Point out each leukocyte.
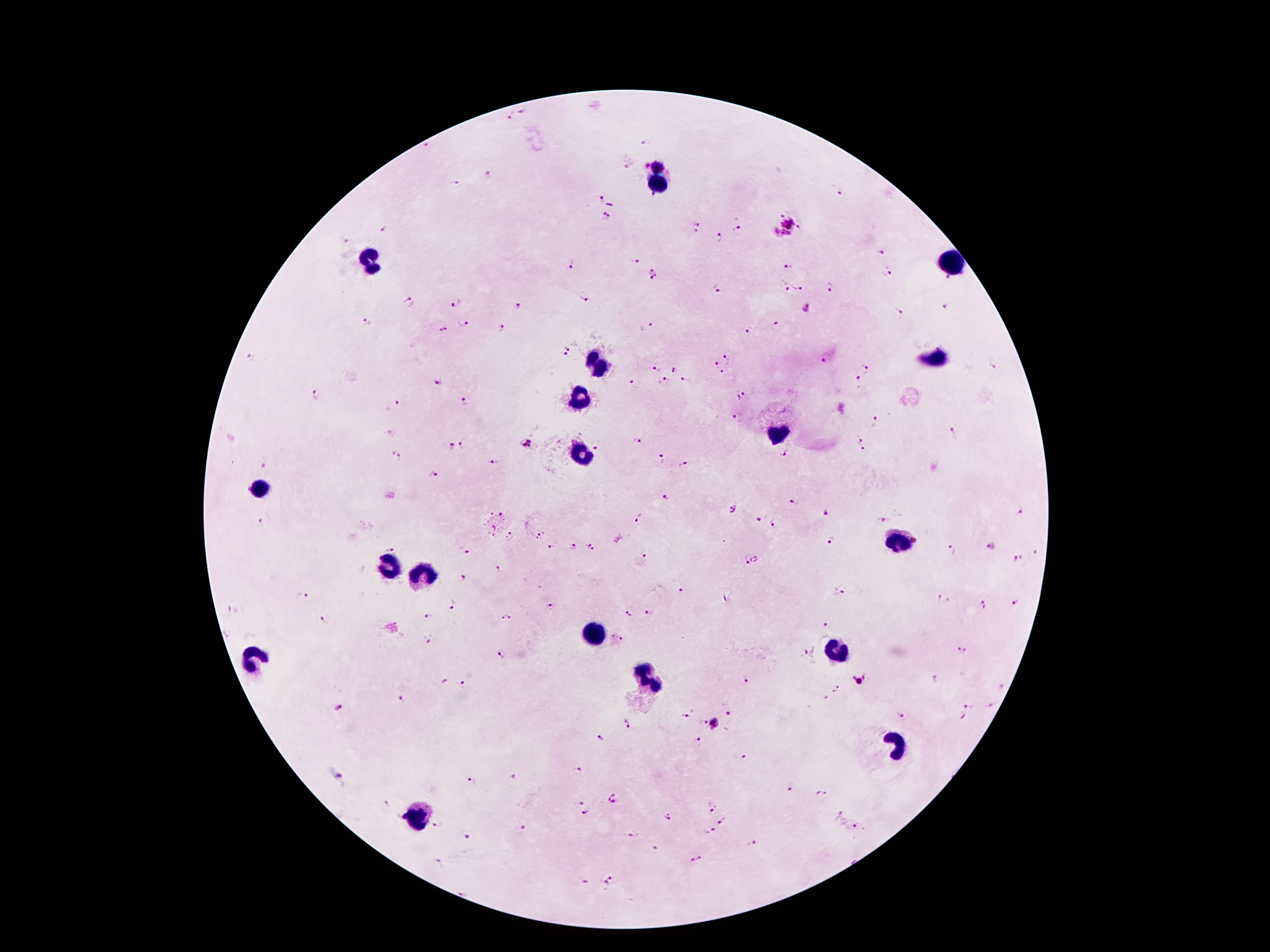

Approximate centers as (x, y) in pixels.
Leukocytes: (658, 184), (369, 260), (950, 263), (936, 360), (598, 363), (577, 398), (778, 434), (581, 454), (260, 487), (898, 539), (388, 565), (420, 574), (593, 635), (835, 651), (253, 656), (644, 677), (896, 745), (420, 817).

Summary:
  - Malaria parasite locations: (523, 111), (509, 117), (643, 141), (427, 145), (658, 168), (487, 177), (455, 181), (600, 201), (604, 216), (781, 216), (788, 225), (799, 227), (697, 228), (737, 228), (384, 230), (721, 237), (344, 241), (881, 252), (635, 261), (571, 266), (789, 268), (887, 273), (656, 275), (947, 280), (784, 285), (797, 288), (830, 288), (717, 289), (584, 299), (409, 303), (457, 304), (517, 306), (944, 306), (807, 309), (899, 314), (464, 323), (778, 323), (366, 324), (647, 326), (442, 329), (502, 331), (749, 332), (569, 346), (563, 356), (727, 356), (253, 358), (824, 358), (715, 364), (992, 367), (655, 369), (866, 369), (673, 370), (720, 372), (436, 379), (683, 380), (855, 380), (664, 381), (633, 383), (316, 396), (741, 396), (465, 403), (395, 406), (736, 418), (875, 422), (955, 434), (859, 440), (636, 441), (526, 443), (462, 444), (596, 446), (451, 447), (393, 451), (863, 451), (784, 454), (399, 457), (658, 460), (492, 462), (683, 465), (264, 466), (432, 473), (668, 497), (791, 502), (737, 510), (829, 513), (1021, 513), (264, 519), (638, 519), (757, 519), (880, 519), (771, 523), (540, 535), (511, 539), (832, 540), (573, 546), (992, 546), (551, 547), (589, 547), (389, 548), (463, 551), (951, 551), (644, 556), (755, 559), (1017, 559), (745, 560), (499, 571), (461, 578), (842, 591), (680, 592), (305, 596), (944, 599), (1014, 601), (454, 605), (983, 605), (549, 608), (232, 612), (629, 613), (649, 613), (428, 615), (506, 618), (326, 622), (825, 623), (620, 638), (428, 639), (961, 647), (500, 654), (807, 654), (859, 679), (933, 680), (746, 681), (466, 684), (1003, 686), (837, 689), (401, 698), (969, 704), (993, 705), (339, 709), (686, 715), (902, 715), (729, 716), (962, 718), (624, 723), (713, 723), (600, 738), (697, 742), (743, 756), (577, 771), (337, 776), (513, 778), (473, 782), (790, 786), (819, 793), (615, 801), (387, 802), (579, 802), (708, 808), (839, 814), (584, 815), (668, 819), (723, 822), (437, 826), (522, 828), (856, 828), (709, 830), (466, 836), (632, 836), (753, 844), (654, 848), (698, 858), (436, 860), (611, 879), (584, 882), (463, 892)
  - Patient malaria status: positive for Plasmodium falciparum
  - Preparation: thick peripheral-blood smear
  - Magnification: 100x
  - Capture: smartphone camera through the microscope eyepiece
  - Stain: Giemsa
  - Field of view: single
  - Image size: 1270×952 pixels